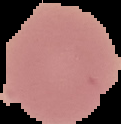
Summary:
  - Malaria status: uninfected
  - Preparation: thin blood smear
  - Image type: segmented cell region on a black background
  - Image size: 121×124 pixels